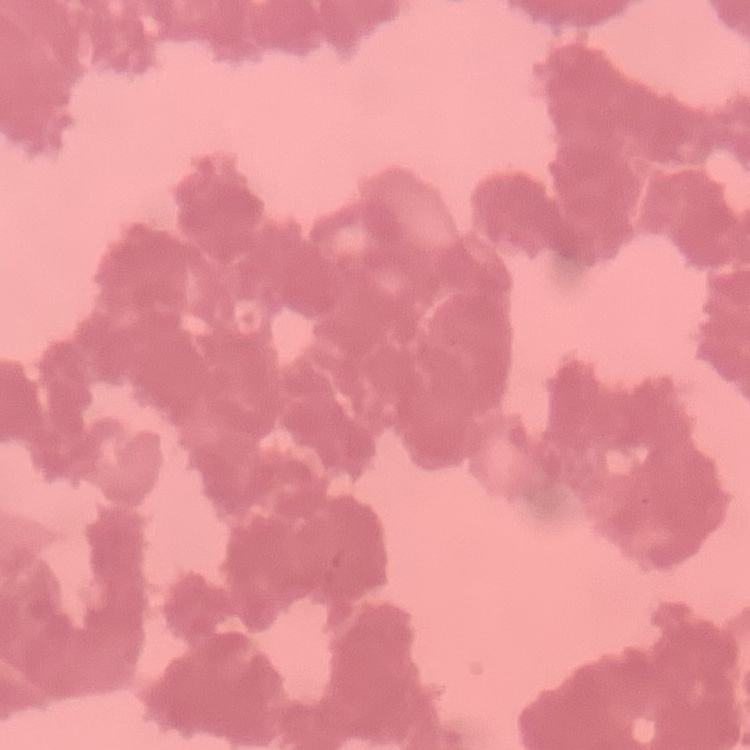

Summary:
  - Erythrocyte morphology: rouleaux formation
  - Image type: one tile cut from a larger photomicrograph
  - Preparation: thin blood smear
  - Stain: Field's or Giemsa